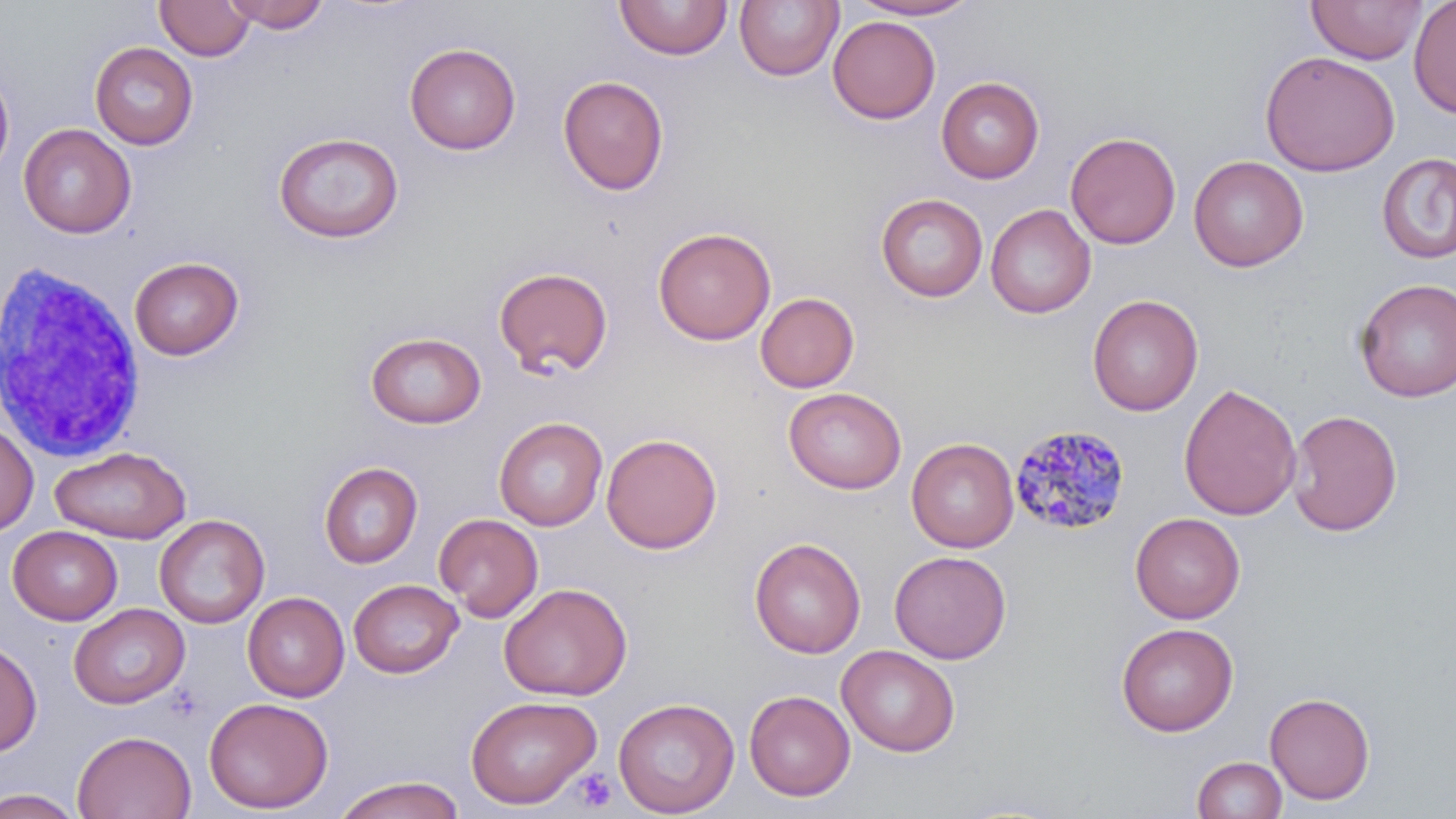
Summary:
  - Coordinate format: approximate bounding boxes as [x1, y1, x2, y2] in pixels
  - White blood cell locations: [0, 253, 146, 460]
  - Uninfected red blood cell locations: [155, 0, 255, 61], [222, 0, 330, 32], [614, 0, 733, 61], [734, 0, 842, 81], [848, 0, 981, 20], [1307, 0, 1427, 64], [1409, 1, 1456, 118], [828, 16, 940, 124], [90, 42, 198, 149], [404, 43, 521, 155], [1260, 50, 1400, 177], [0, 68, 15, 180], [558, 75, 669, 195], [936, 77, 1043, 183], [19, 123, 136, 238], [1066, 131, 1182, 249], [273, 132, 404, 243], [1377, 153, 1456, 264], [1189, 155, 1308, 272], [875, 193, 988, 302], [985, 203, 1096, 319], [653, 227, 776, 345], [129, 256, 244, 360], [494, 266, 613, 377], [1354, 278, 1456, 403], [755, 291, 859, 393], [1087, 294, 1203, 415], [365, 331, 486, 428], [1178, 383, 1302, 520], [783, 387, 906, 494], [1287, 409, 1402, 536], [494, 416, 608, 530], [0, 421, 38, 537], [601, 433, 722, 554], [906, 437, 1019, 553], [50, 446, 192, 543], [318, 461, 422, 569], [1130, 512, 1246, 624], [434, 513, 543, 622], [154, 514, 269, 628], [8, 526, 122, 625], [750, 537, 866, 658], [889, 550, 1011, 663], [348, 578, 464, 678], [498, 582, 632, 701], [243, 591, 349, 702], [69, 602, 190, 709], [1116, 622, 1238, 736], [0, 638, 42, 757], [837, 645, 960, 756], [744, 689, 855, 801], [1265, 692, 1375, 804], [465, 695, 601, 809], [204, 697, 334, 814], [614, 697, 739, 818], [72, 730, 196, 818], [1192, 755, 1288, 819], [333, 775, 465, 819], [0, 788, 84, 818]
  - Plasmodium malariae-infected red blood cell locations: [1009, 423, 1131, 535]
  - Platelet locations: [572, 768, 616, 811]
  - Slide-level diagnosis: Plasmodium malariae
  - Preparation: thin blood smear
  - Stain: May-Grünwald-Giemsa
  - Magnification: 1000x
  - Image size: 1456×819 pixels
  - Field of view: single
  - Modality: light microscopy